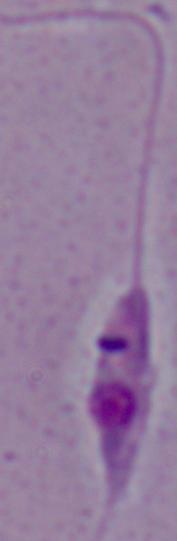
magnification: 1000x
identification: Leishmania
modality: photomicrograph